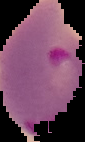
image size = 85×142 pixels
result = malaria parasites identified
preparation = thin blood film
image type = cell region segmented out of the field of view; surrounding area masked to black